Locate every white blood cell.
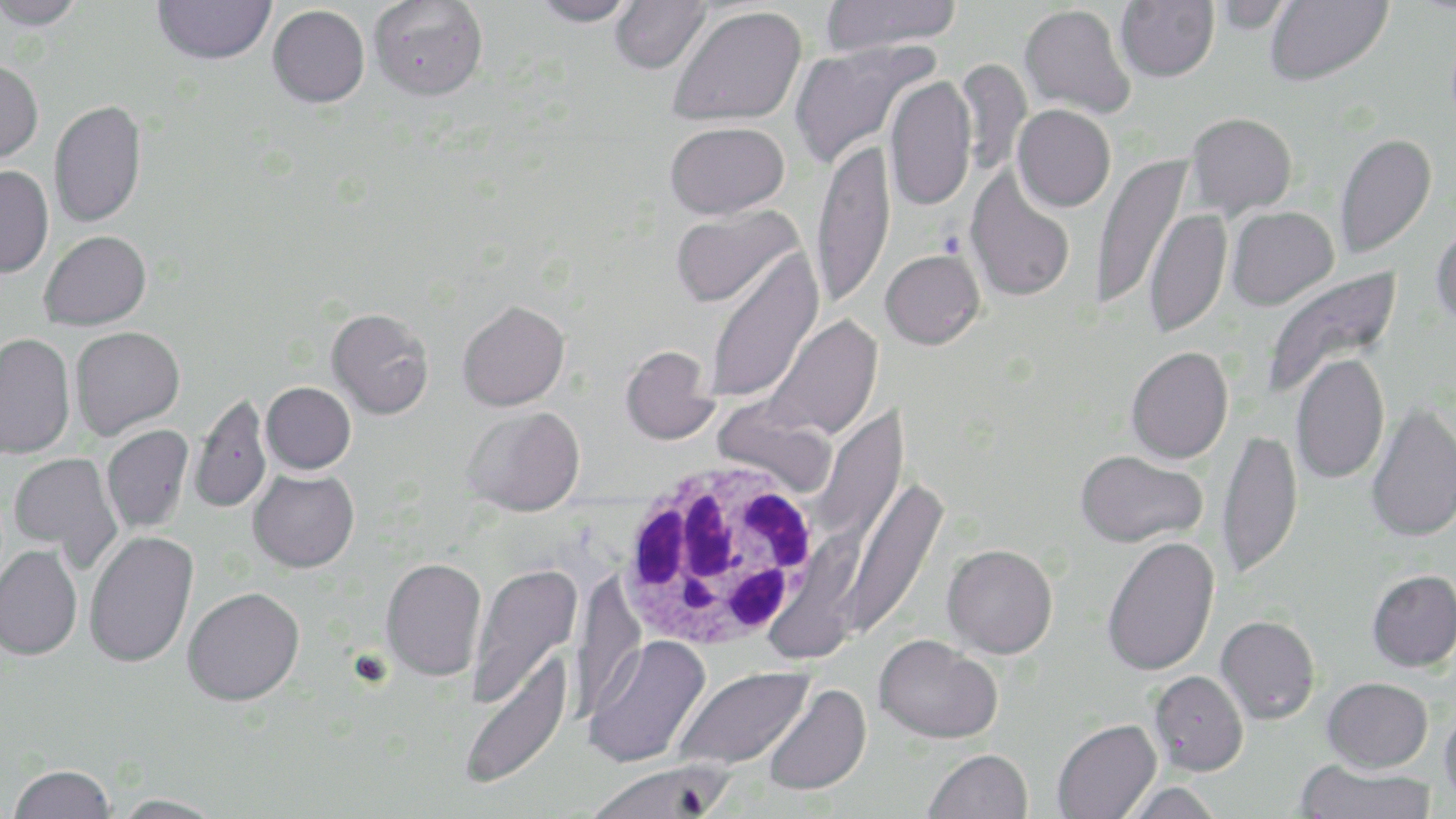

Approximate bounding boxes as [x1, y1, x2, y2] in pixels.
White blood cells: [614, 454, 827, 656].

Uninfected red blood cell locations: [0, 0, 86, 31], [152, 0, 275, 64], [368, 0, 488, 100], [532, 0, 639, 27], [610, 0, 711, 74], [820, 0, 962, 55], [1115, 0, 1219, 82], [1264, 0, 1392, 86], [1211, 1, 1294, 33], [1019, 4, 1135, 119], [268, 5, 369, 107], [667, 5, 806, 127], [789, 39, 936, 172], [956, 58, 1032, 178], [0, 60, 43, 165], [884, 75, 976, 212], [49, 99, 147, 228], [1012, 104, 1116, 212], [1185, 112, 1298, 218], [664, 121, 789, 219], [1335, 133, 1437, 258], [811, 140, 895, 307], [1091, 156, 1191, 311], [0, 166, 53, 278], [965, 167, 1075, 302], [669, 206, 803, 308], [1226, 206, 1338, 310], [1143, 208, 1231, 338], [1431, 217, 1456, 328], [39, 230, 151, 330], [704, 248, 823, 405], [880, 249, 985, 349], [1260, 267, 1402, 401], [457, 300, 570, 411], [326, 308, 433, 419], [765, 315, 882, 440], [69, 326, 185, 440], [0, 333, 75, 458], [620, 345, 717, 445], [1126, 346, 1233, 463], [1290, 353, 1390, 485], [261, 382, 356, 474], [189, 392, 271, 513], [1365, 401, 1456, 543], [811, 406, 909, 549], [462, 407, 585, 516], [101, 424, 194, 533], [1217, 427, 1303, 579], [1075, 449, 1207, 547], [9, 452, 123, 568], [248, 469, 359, 572], [839, 477, 947, 642], [84, 530, 198, 667], [1101, 536, 1220, 676], [942, 543, 1058, 658], [0, 544, 83, 659], [380, 557, 487, 681], [466, 563, 583, 708], [1367, 570, 1456, 672], [182, 587, 304, 706], [1216, 615, 1321, 725], [584, 635, 711, 769], [874, 635, 1003, 744], [458, 649, 574, 791], [673, 666, 813, 771], [1149, 670, 1249, 775], [1322, 676, 1433, 772], [762, 683, 871, 796], [1439, 700, 1456, 809], [1051, 719, 1161, 819], [923, 748, 1033, 819], [1295, 760, 1436, 819], [586, 761, 735, 819], [7, 764, 116, 819], [1119, 782, 1224, 819], [110, 794, 227, 819]. Slide-level diagnosis: Plasmodium falciparum. Optical microscopy. Single field of view. 1000x magnification. Image is 1456×819 pixels. May-Grünwald-Giemsa-stained preparation. Thin blood film.